Name the blood parasite species.
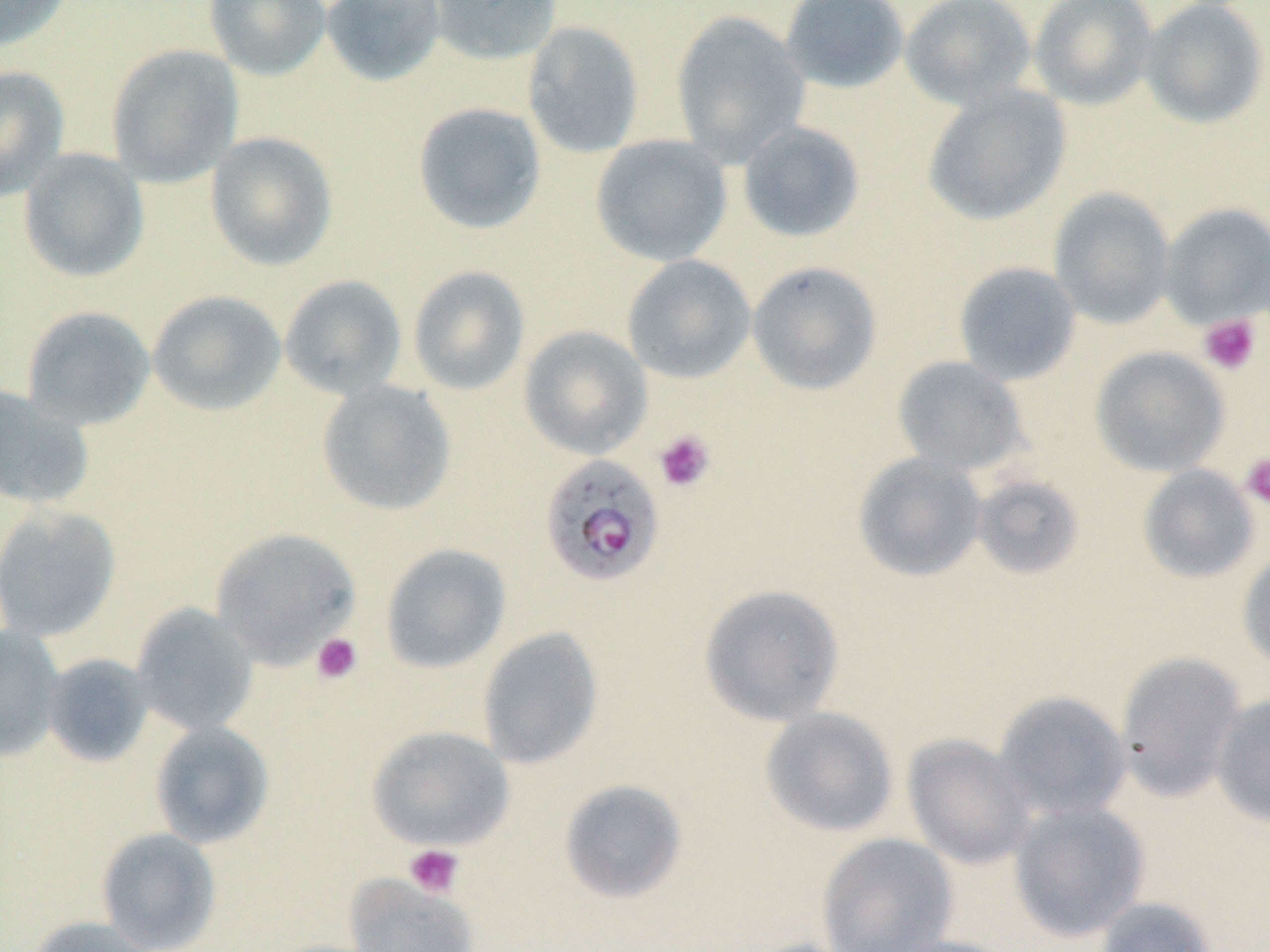

Plasmodium falciparum.

Summary:
  - Coordinate format: approximate bounding boxes as named x1/y1/x2/y2 corners in pixels
  - Plasmodium falciparum-infected red blood cell locations: (x1=539, y1=454, x2=665, y2=588)
  - Uninfected red blood cell locations: (x1=0, y1=0, x2=72, y2=52), (x1=204, y1=0, x2=331, y2=80), (x1=320, y1=0, x2=446, y2=88), (x1=425, y1=0, x2=562, y2=67), (x1=779, y1=0, x2=910, y2=94), (x1=899, y1=0, x2=1037, y2=110), (x1=1028, y1=0, x2=1159, y2=110), (x1=1138, y1=0, x2=1269, y2=129), (x1=670, y1=11, x2=811, y2=166), (x1=522, y1=21, x2=644, y2=159), (x1=106, y1=44, x2=243, y2=188), (x1=0, y1=65, x2=70, y2=202), (x1=921, y1=84, x2=1071, y2=226), (x1=412, y1=102, x2=547, y2=235), (x1=736, y1=121, x2=865, y2=243), (x1=205, y1=131, x2=339, y2=271), (x1=590, y1=134, x2=733, y2=267), (x1=18, y1=148, x2=149, y2=283), (x1=1048, y1=188, x2=1176, y2=329), (x1=1158, y1=203, x2=1270, y2=328), (x1=621, y1=254, x2=756, y2=384), (x1=746, y1=261, x2=883, y2=395), (x1=953, y1=261, x2=1081, y2=385), (x1=407, y1=265, x2=531, y2=395), (x1=279, y1=274, x2=407, y2=399), (x1=147, y1=289, x2=287, y2=416), (x1=20, y1=305, x2=155, y2=431), (x1=518, y1=325, x2=652, y2=459), (x1=1089, y1=346, x2=1229, y2=477), (x1=891, y1=355, x2=1029, y2=476), (x1=316, y1=379, x2=457, y2=516), (x1=0, y1=384, x2=94, y2=509), (x1=853, y1=451, x2=987, y2=582), (x1=1137, y1=464, x2=1260, y2=584), (x1=970, y1=474, x2=1085, y2=580), (x1=0, y1=504, x2=121, y2=642), (x1=210, y1=527, x2=362, y2=668), (x1=380, y1=543, x2=512, y2=674), (x1=1237, y1=546, x2=1270, y2=672), (x1=698, y1=584, x2=844, y2=726), (x1=130, y1=602, x2=259, y2=736), (x1=0, y1=625, x2=65, y2=763), (x1=477, y1=626, x2=604, y2=769), (x1=1115, y1=651, x2=1247, y2=802), (x1=41, y1=653, x2=154, y2=767), (x1=992, y1=690, x2=1131, y2=823), (x1=1211, y1=693, x2=1270, y2=827), (x1=759, y1=707, x2=899, y2=837), (x1=149, y1=720, x2=274, y2=849), (x1=366, y1=725, x2=515, y2=851), (x1=902, y1=734, x2=1035, y2=869), (x1=558, y1=778, x2=688, y2=904), (x1=1008, y1=801, x2=1149, y2=942), (x1=96, y1=827, x2=222, y2=952), (x1=817, y1=832, x2=958, y2=952), (x1=344, y1=875, x2=478, y2=952), (x1=1094, y1=896, x2=1217, y2=952), (x1=28, y1=916, x2=156, y2=952), (x1=878, y1=934, x2=1020, y2=952)
  - Platelet locations: (x1=1198, y1=314, x2=1261, y2=375), (x1=653, y1=430, x2=715, y2=492), (x1=1240, y1=453, x2=1270, y2=512), (x1=311, y1=632, x2=363, y2=685), (x1=404, y1=844, x2=464, y2=898)
  - Preparation: thin blood smear
  - Stain: May-Grünwald-Giemsa
  - Magnification: 1000x
  - Modality: optical microscopy
  - Field of view: single
  - Image size: 1270×952 pixels